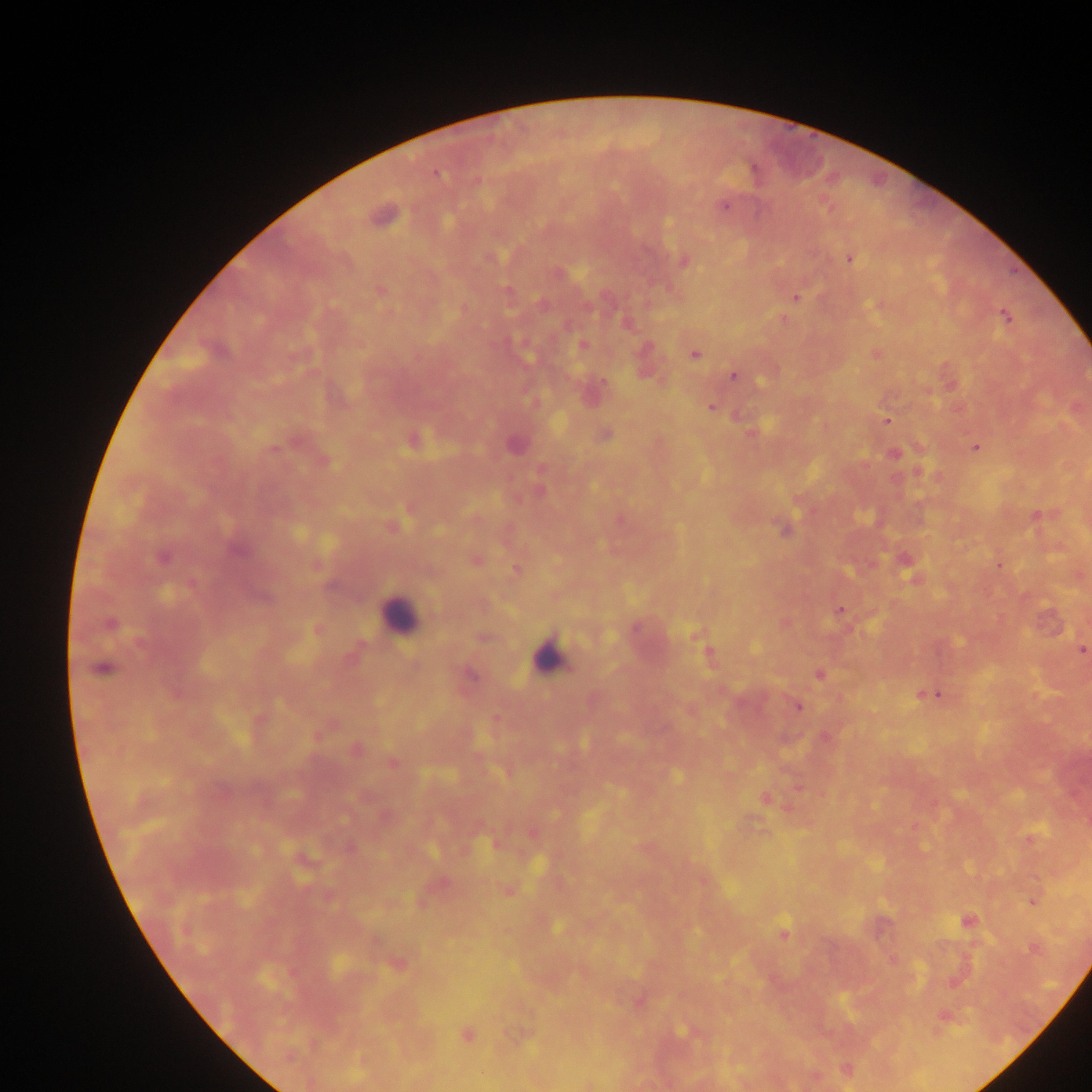

Approximate centers as (x, y) in pixels. Malaria parasite locations: (435, 173), (476, 181), (724, 205), (383, 215), (849, 258), (683, 260), (380, 290), (795, 297), (542, 304), (880, 304), (461, 309), (1005, 316), (782, 319), (626, 323), (582, 345), (875, 353), (694, 354), (645, 362), (733, 375), (949, 382), (590, 390), (710, 407), (887, 419), (751, 432), (605, 434), (413, 440), (515, 445), (976, 447), (893, 453), (323, 460), (918, 472), (800, 500), (409, 509), (1037, 515), (619, 519), (391, 526), (784, 528), (162, 556), (475, 560), (317, 565), (999, 565), (908, 567), (515, 569), (913, 576), (840, 609), (785, 623), (109, 624), (635, 628), (317, 629), (696, 634), (483, 637), (1081, 650), (707, 652), (102, 668), (468, 674), (819, 674), (930, 693), (797, 706), (496, 718), (326, 727), (824, 737), (354, 749), (391, 762), (798, 786), (765, 798), (386, 817), (532, 833), (1030, 838), (496, 843), (703, 880), (439, 883), (508, 890), (1032, 901), (966, 921), (784, 933), (1033, 948), (892, 960), (398, 964), (638, 1000), (944, 1015), (686, 1031), (466, 1035), (846, 1069), (814, 1076), (588, 1084). Leukocyte locations: (399, 618), (547, 657). Sample from Ghana. Image is 1092×1092 pixels. One field of view. Photographed through a microscope with a mobile-phone camera. Thick blood film.